Describe the morphology of the red blood cells.
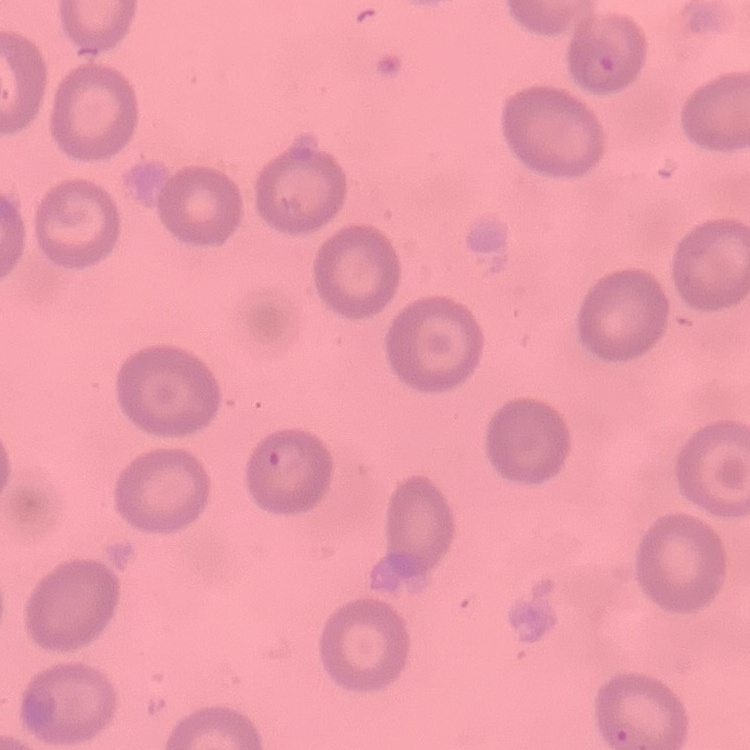
They show no rouleaux formation.

Thin blood smear. Square crop of a larger photomicrograph. Field's or Giemsa stain.